Evaluate for malaria.
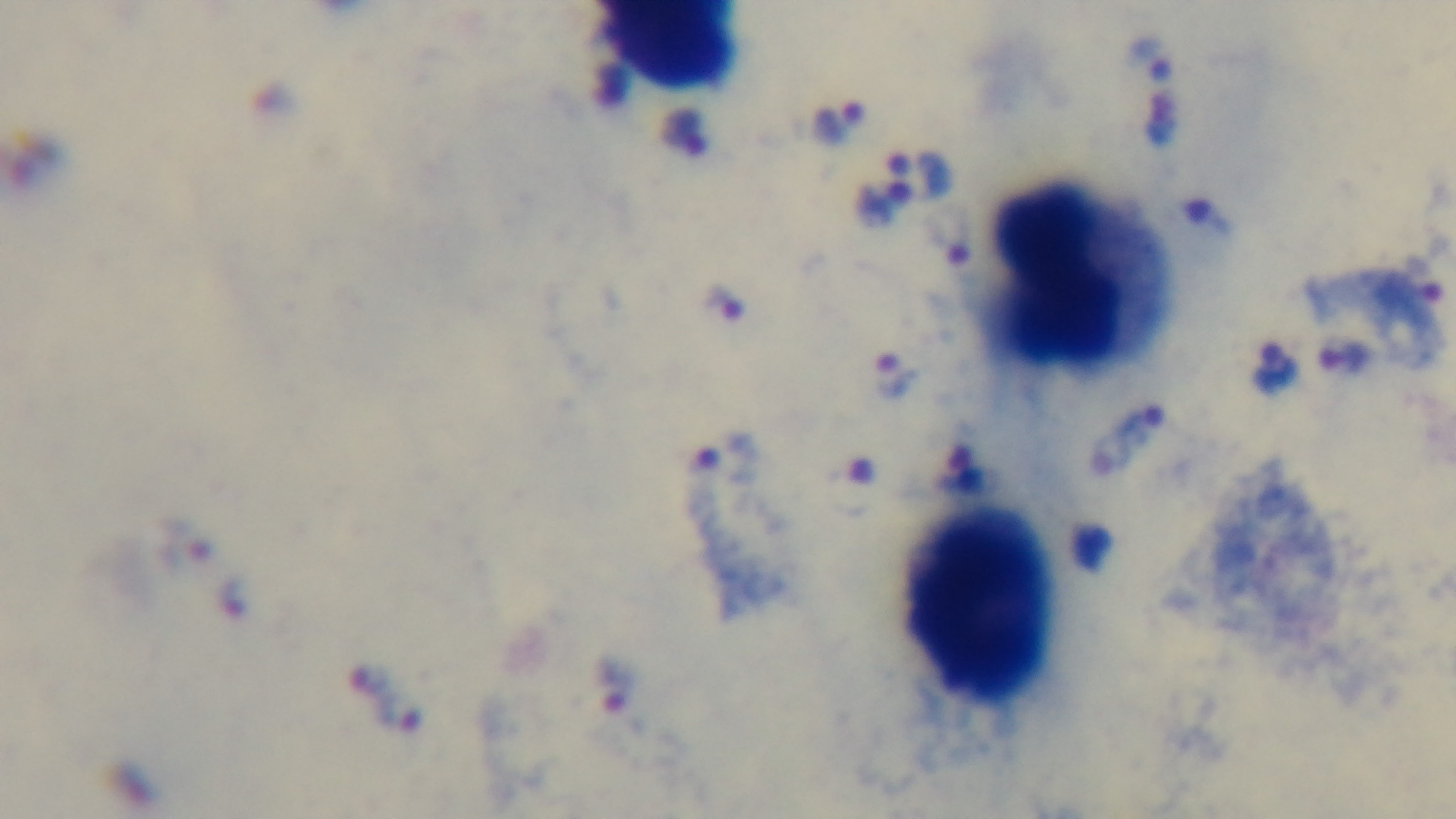
Infected.

objective = 100x oil immersion
field of view = single
preparation = thick
modality = light microscopy
stain = Giemsa
capture = mounted 4K digital camera